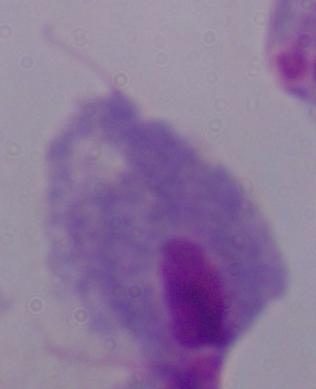
Photomicrograph. 1000x magnification. A trichomonad is seen.